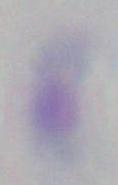
Toxoplasma gondii is seen. Captured at 1000x magnification. Micrograph.